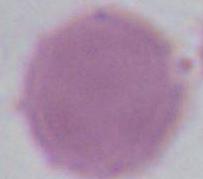
identification = red blood cell
modality = micrograph
magnification = 1000x